Look for Plasmodium parasites.
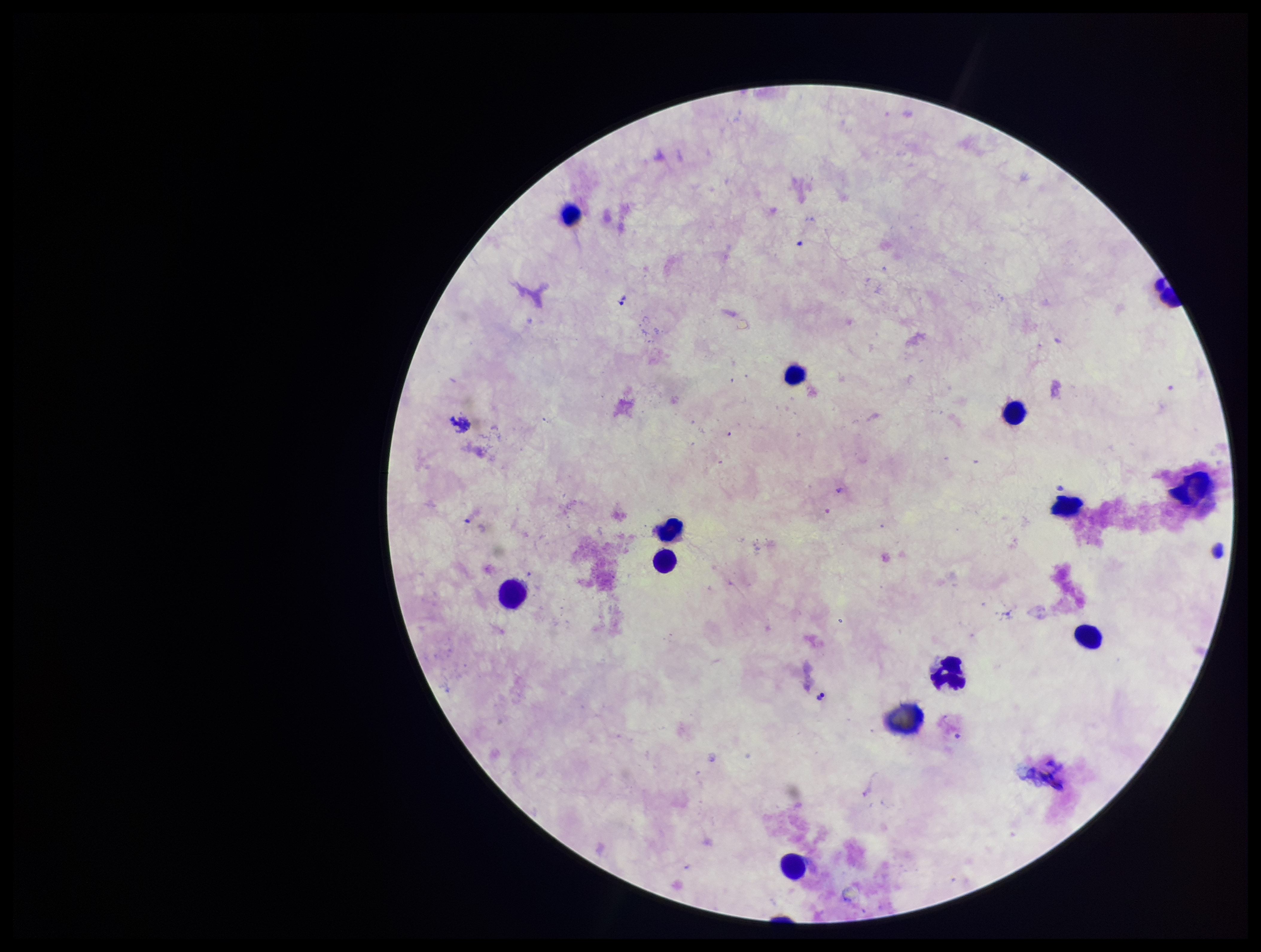

None identified.

Summary:
  - Parasite count: 0
  - Patient malaria status: negative
  - Image size: 1261×952 pixels
  - Preparation: thick blood smear
  - Leukocyte count: 12
  - Field of view: one from this slide
  - Stain: Giemsa
  - Capture: smartphone photograph through the microscope eyepiece